Comment on the morphology of the red blood cells.
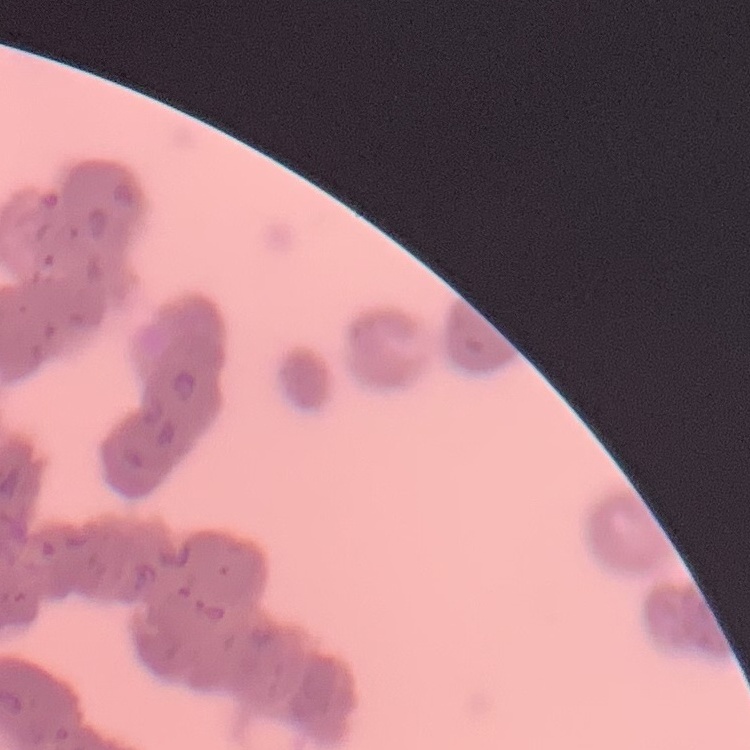
Rouleaux formation.

One tile cut from a larger photomicrograph. Thin blood smear. Field's or Giemsa stain.